State the blood parasite species.
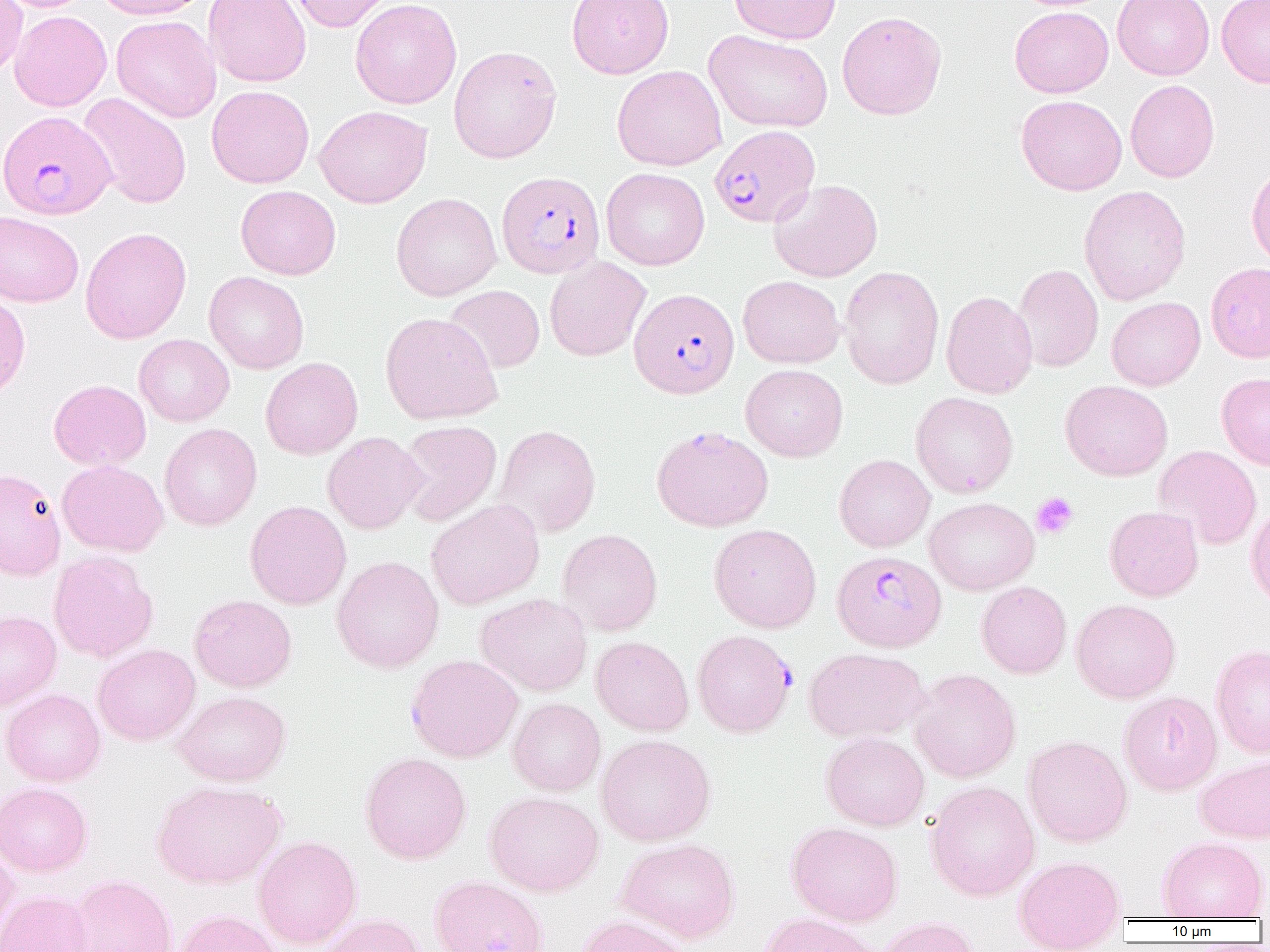

Plasmodium falciparum.

Approximate bounding boxes as (x1, y1, x2, y2) in pixels. Plasmodium falciparum-infected red blood cell locations (subset): (0, 110, 116, 220), (710, 125, 819, 229), (497, 170, 605, 278), (629, 288, 740, 399), (832, 550, 947, 651), (693, 629, 796, 737). Uninfected red blood cell locations (subset): (0, 0, 95, 12), (0, 0, 27, 77), (94, 0, 210, 19), (203, 0, 311, 87), (285, 0, 396, 32), (350, 0, 462, 109), (566, 0, 674, 79), (729, 0, 841, 44), (1113, 0, 1214, 80), (1216, 0, 1270, 88), (1009, 6, 1113, 97), (9, 10, 112, 111), (837, 11, 947, 120), (111, 15, 221, 123), (704, 29, 833, 133), (448, 45, 562, 163), (612, 65, 727, 171), (1125, 80, 1219, 182), (207, 85, 314, 188), (79, 93, 192, 208), (1016, 95, 1127, 195), (314, 105, 432, 208), (1246, 161, 1270, 270), (601, 168, 710, 270), (769, 179, 883, 282), (235, 185, 341, 280), (1078, 185, 1191, 305), (391, 192, 502, 301), (0, 211, 84, 308), (80, 227, 192, 344), (544, 256, 651, 361), (1205, 262, 1270, 363), (1012, 263, 1104, 373), (839, 266, 944, 389), (203, 271, 309, 374), (738, 276, 845, 368), (443, 285, 545, 374), (0, 291, 31, 401), (941, 291, 1038, 399), (1106, 297, 1205, 390), (380, 312, 503, 424), (134, 334, 234, 426), (261, 357, 363, 459), (741, 364, 848, 462), (1217, 372, 1270, 471), (49, 379, 151, 470), (1060, 380, 1173, 480), (910, 392, 1018, 498), (396, 420, 502, 526), (160, 423, 262, 531), (494, 424, 601, 537), (322, 431, 427, 534), (1154, 445, 1262, 550), (834, 454, 935, 552), (57, 460, 168, 556), (0, 467, 66, 580), (924, 497, 1039, 595), (426, 499, 544, 610), (244, 500, 352, 609), (1246, 501, 1270, 609), (1104, 506, 1203, 601), (709, 523, 821, 632), (557, 528, 663, 636), (48, 550, 157, 663), (332, 555, 444, 673), (976, 581, 1071, 679), (475, 592, 593, 696), (189, 594, 297, 692), (1071, 599, 1180, 703), (0, 610, 61, 711), (591, 636, 694, 736), (93, 643, 200, 746), (1211, 644, 1270, 758), (803, 647, 929, 742), (405, 654, 523, 762), (908, 668, 1021, 784), (1, 688, 105, 786), (173, 691, 291, 786), (1119, 691, 1222, 795), (508, 698, 606, 796), (821, 732, 929, 830), (596, 734, 716, 846), (1023, 735, 1132, 847), (360, 752, 471, 864), (1194, 754, 1270, 843), (151, 780, 286, 889), (925, 781, 1040, 901), (0, 782, 92, 876), (484, 790, 604, 896), (786, 822, 903, 926), (253, 836, 362, 948), (1158, 836, 1268, 920), (615, 838, 740, 943), (0, 841, 19, 946), (1013, 855, 1126, 950), (68, 873, 178, 952), (429, 875, 549, 952), (0, 890, 93, 952), (171, 909, 281, 952), (319, 913, 425, 952), (757, 913, 880, 952), (576, 915, 693, 952), (877, 917, 981, 952). Platelet locations: (1032, 492, 1078, 539). Image is 1270×952 pixels. Single field of view. Thin blood smear. 1000x magnification. Optical microscopy.